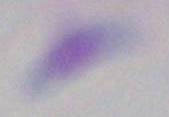
Toxoplasma gondii is shown. Photomicrograph. Captured at 1000x magnification.